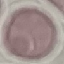

Malaria status: uninfected. Acquired by smartphone through the microscope eyepiece. Thin blood smear. Giemsa-stained preparation. Automatically extracted cell patch, resized to 64 × 64 pixels.